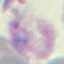

Summary:
  - Result: malaria parasites detected
  - Image type: cell patch, automatically extracted from a larger field of view and resized to 64 × 64 pixels
  - Preparation: thin blood film
  - Stain: Giemsa
  - Capture: smartphone through the microscope eyepiece